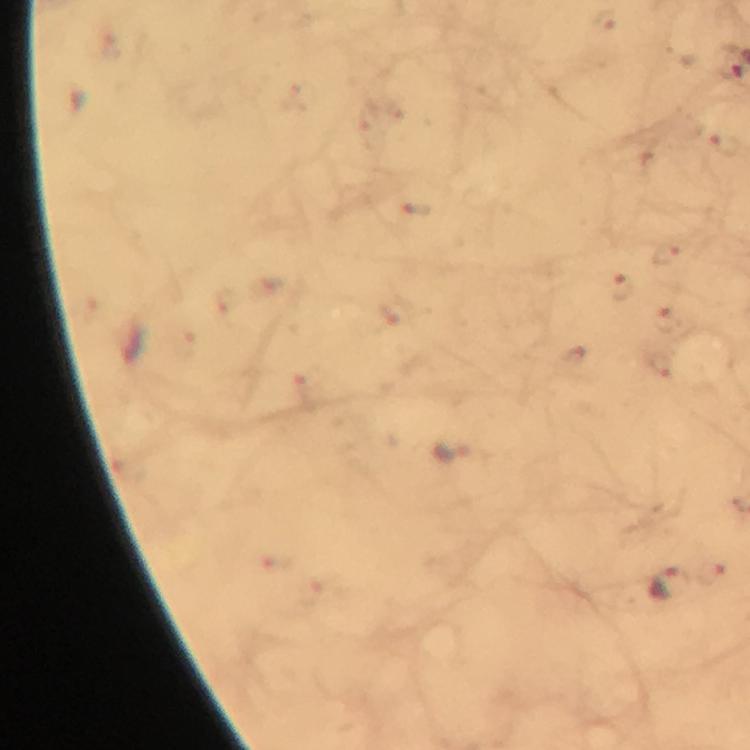 Approximate centers as {x, y} in pixels. Plasmodium parasite locations: {622, 284}, {668, 586}. Thick blood smear. Image is 750×750 pixels. At 100x magnification. Cropped region of a single field of view. From a diagnostic examination for malaria. Immersion oil applied. Giemsa-stained preparation. Smartphone photograph taken through a microscope.